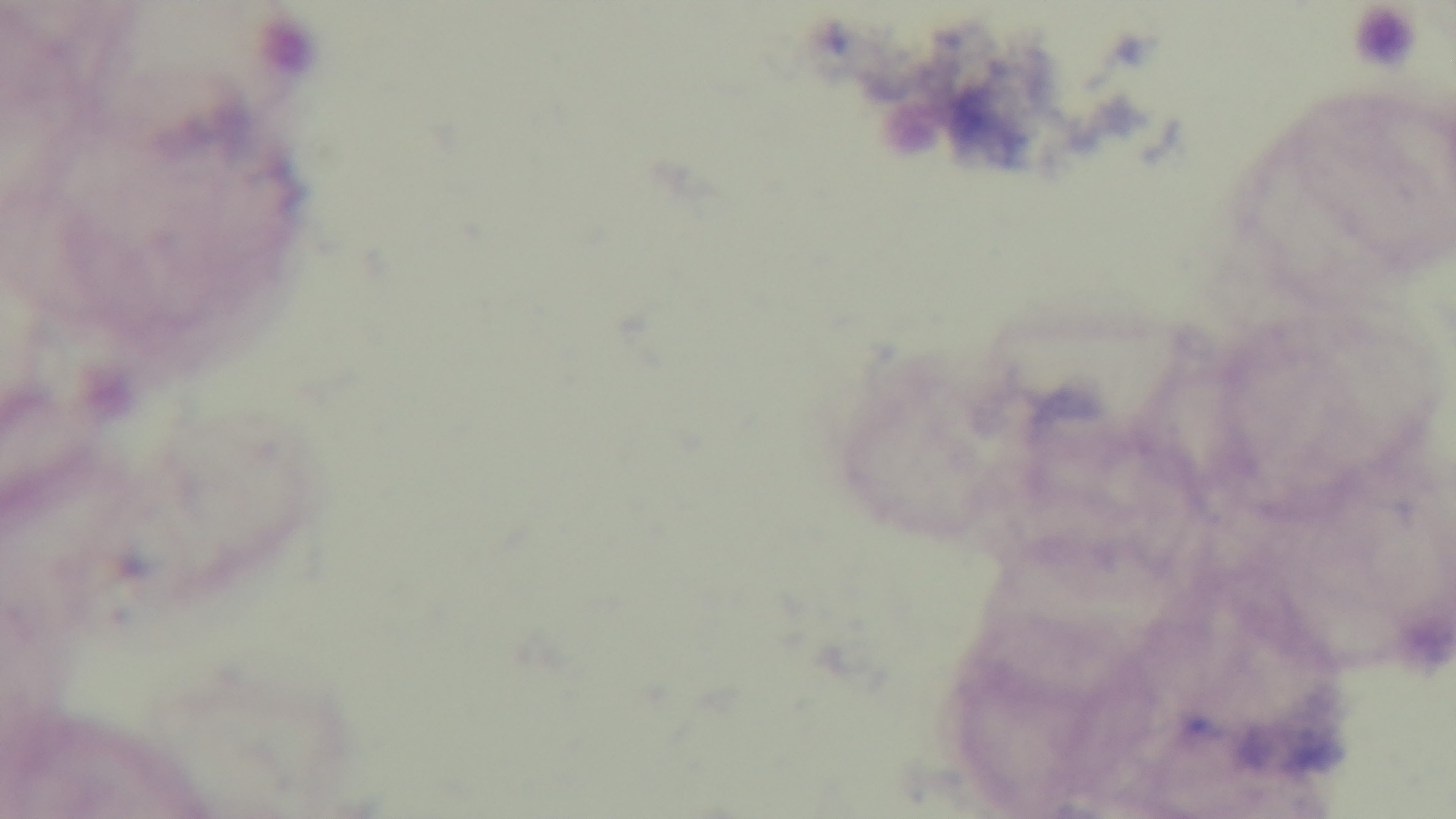
Summary:
  - Objective: 100x oil immersion
  - Capture: mounted 4K digital camera
  - Malaria status: negative
  - Stain: Giemsa
  - Preparation: thick smear
  - Modality: light microscopy
  - Field of view: single